Assess this cell for malaria.
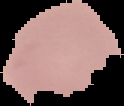

Uninfected.

Segmented cell region on a black background. From a thin blood smear. Image is 124×106 pixels.